State which parasite is depicted.
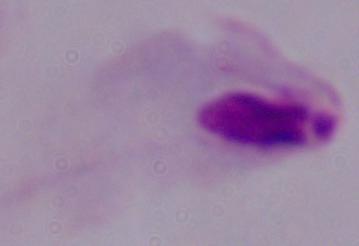

This is a trichomonad.

Captured at 1000x magnification. Micrograph.